Report the malaria status of this cell.
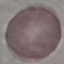
It is uninfected.

Summary:
  - Stain: Giemsa
  - Image type: cell patch, automatically extracted from a larger field of view and resized to 64 × 64 pixels
  - Preparation: thin smear
  - Capture: smartphone camera at the microscope eyepiece